Locate and identify every blood parasite.
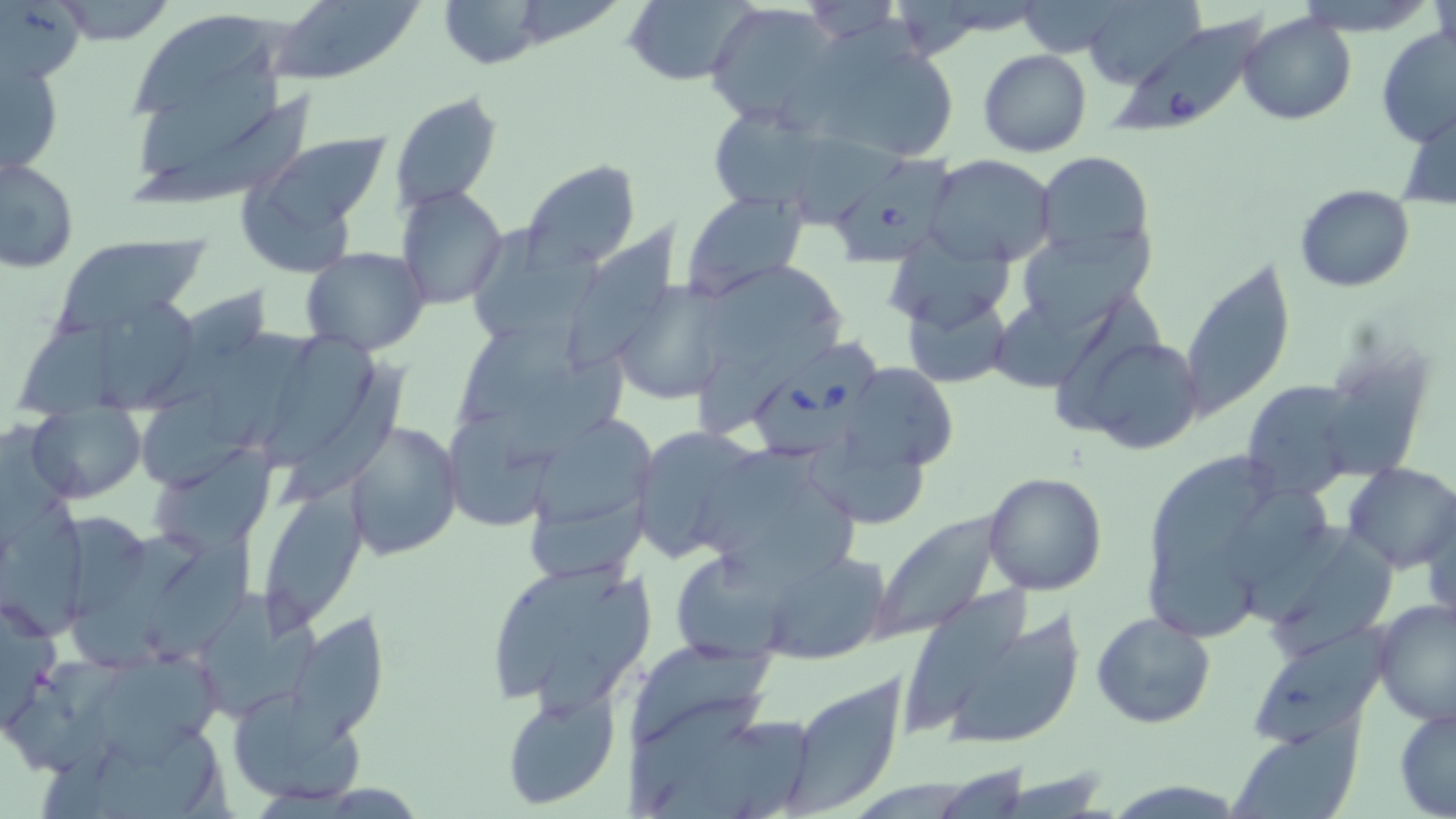

Approximate bounding boxes as [x1, y1, x2, y2] in pixels.
Babesia divergens-infected red blood cells: [1106, 16, 1277, 142], [835, 151, 957, 271], [751, 341, 886, 462].
No Plasmodium falciparum, Plasmodium ovale, Plasmodium malariae, Plasmodium vivax, or Trypanosoma brucei observed.

Uninfected red blood cell locations: [0, 0, 94, 78], [434, 0, 553, 68], [620, 0, 756, 87], [1083, 0, 1203, 88], [52, 1, 179, 46], [268, 1, 422, 85], [1013, 1, 1134, 57], [706, 3, 844, 128], [125, 10, 290, 126], [1240, 12, 1356, 126], [1377, 26, 1456, 150], [799, 30, 958, 165], [978, 49, 1092, 158], [2, 54, 65, 176], [126, 78, 320, 209], [389, 92, 503, 213], [1399, 103, 1455, 212], [709, 108, 828, 202], [791, 126, 909, 230], [235, 133, 388, 272], [1033, 151, 1156, 262], [924, 154, 1058, 267], [2, 158, 78, 273], [520, 161, 640, 271], [1295, 184, 1415, 292], [394, 186, 508, 309], [682, 190, 809, 302], [569, 223, 682, 375], [465, 226, 603, 349], [1017, 229, 1152, 334], [52, 233, 203, 334], [301, 247, 433, 355], [1179, 258, 1294, 428], [701, 263, 843, 382], [610, 277, 730, 405], [140, 289, 273, 416], [903, 290, 1013, 389], [96, 296, 204, 410], [18, 306, 159, 421], [201, 320, 329, 449], [461, 320, 587, 419], [1077, 332, 1205, 455], [1315, 348, 1435, 486], [503, 354, 626, 479], [284, 359, 409, 512], [844, 361, 959, 476], [1240, 378, 1361, 500], [442, 406, 566, 530], [30, 408, 146, 503], [532, 417, 658, 523], [345, 421, 463, 561], [629, 423, 763, 562], [806, 432, 939, 523], [148, 449, 270, 555], [1153, 452, 1291, 583], [1343, 462, 1456, 574], [530, 464, 663, 581], [714, 469, 867, 596], [981, 471, 1107, 594], [257, 487, 369, 631], [1228, 487, 1332, 590], [1422, 494, 1456, 632], [2, 504, 89, 636], [873, 513, 1001, 639], [68, 525, 209, 677], [145, 525, 258, 664], [1264, 536, 1406, 660], [1136, 542, 1263, 645], [760, 551, 890, 665], [671, 552, 792, 663], [478, 557, 655, 716], [906, 581, 1032, 734], [205, 589, 325, 710], [0, 594, 61, 737], [1373, 597, 1456, 726], [279, 609, 388, 770], [1091, 612, 1216, 730], [948, 614, 1085, 742], [1246, 623, 1392, 746], [627, 640, 779, 747], [100, 658, 226, 768], [782, 676, 908, 812], [226, 686, 368, 805], [499, 688, 621, 812], [625, 692, 767, 815], [1394, 706, 1456, 817], [1231, 724, 1362, 819], [1106, 779, 1245, 816]. Slide-level diagnosis: Babesia divergens. Image is 1456×819 pixels. Captured at 1000x magnification. One field of a larger specimen. Light microscopy. May-Grünwald-Giemsa-stained preparation. Thin blood film.